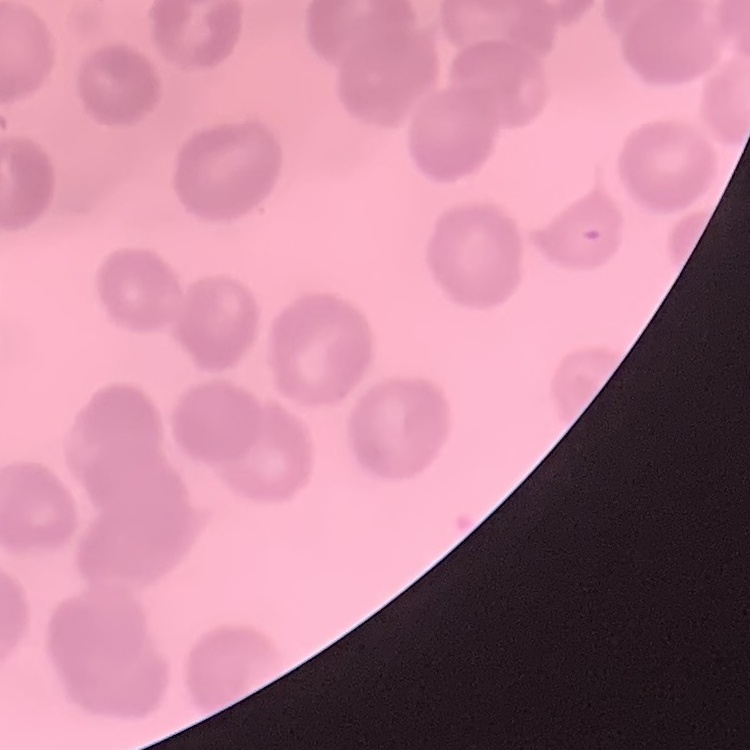
Summary:
  - Red blood cell morphology: no rouleaux formation
  - Preparation: thin peripheral smear
  - Stain: Field's or Giemsa
  - Image type: one tile cut from a larger photomicrograph